Report the malaria status of this cell.
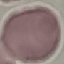
It is uninfected.

Photographed with a smartphone camera at the microscope eyepiece. Automatically extracted cell patch, resized to 64 × 64 pixels. Giemsa-stained preparation. Thin blood film.